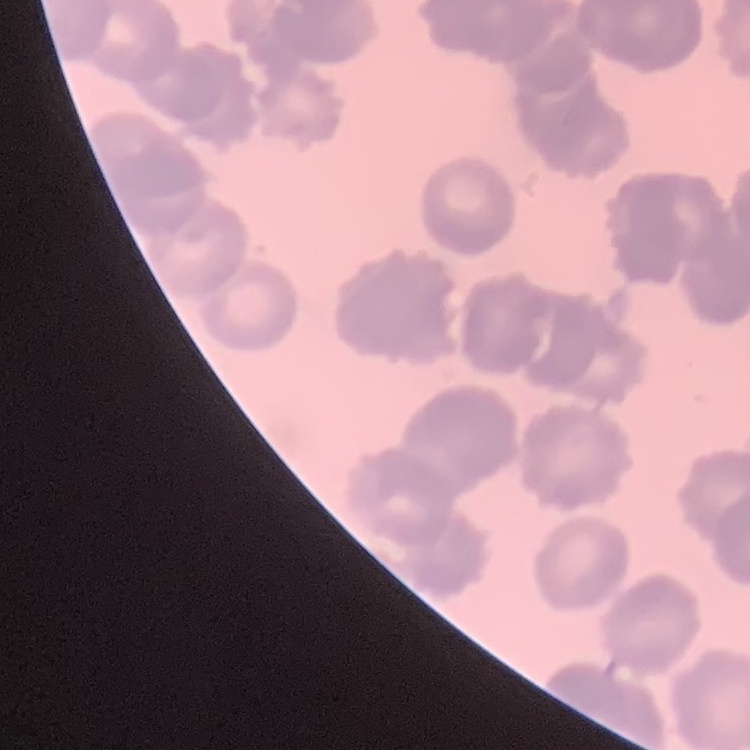

The red blood cells show rouleaux formation. One tile cut from a larger photomicrograph. Stained with either Field's or Giemsa. Thin blood film.